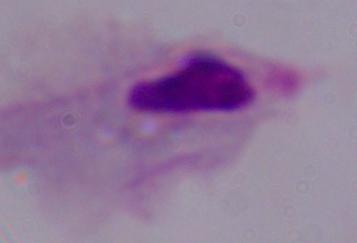 1000x magnification. Micrograph. A trichomonad is shown.